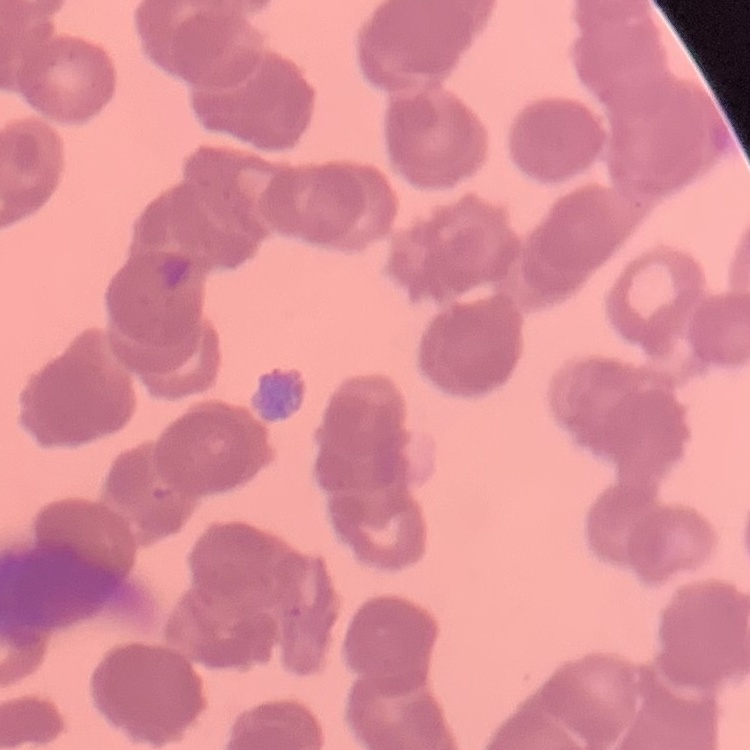
The erythrocytes exhibit rouleaux formation. Thin peripheral smear. Stained with either Field's or Giemsa. Square crop of a larger photomicrograph.